Report the malaria status of this cell.
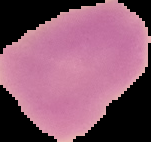
It is uninfected.

Image is 151×142 pixels. From a thin blood film. The area outside the segmented cell region is set to black.